Describe the morphology of the red blood cells.
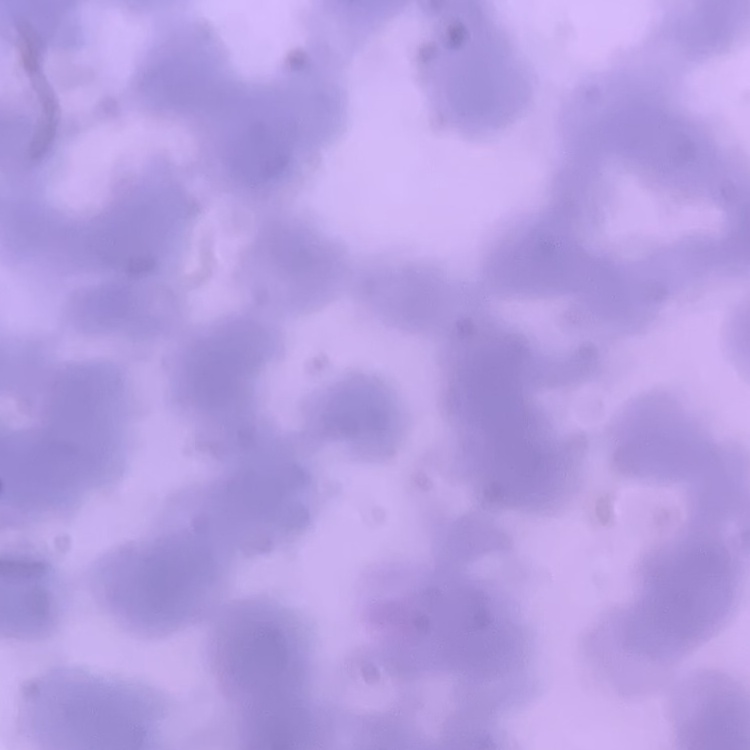

Rouleaux formation.

Summary:
  - Preparation: thin blood smear
  - Stain: Field's or Giemsa
  - Image type: square crop of a larger photomicrograph